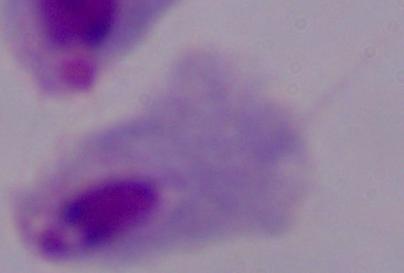

Summary:
  - Identification: trichomonad
  - Modality: photomicrograph
  - Magnification: 1000x